Report the malaria status of this cell.
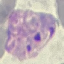

Parasitized.

image_type: automatically extracted cell patch, resized to 64 × 64 pixels
capture: smartphone through the microscope eyepiece
preparation: thin blood film
stain: Giemsa